Report the malaria status of this cell.
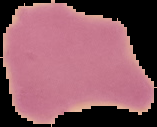

Uninfected.

Image is 157×127 pixels. The area outside the segmented cell region is set to black. From a thin blood smear.